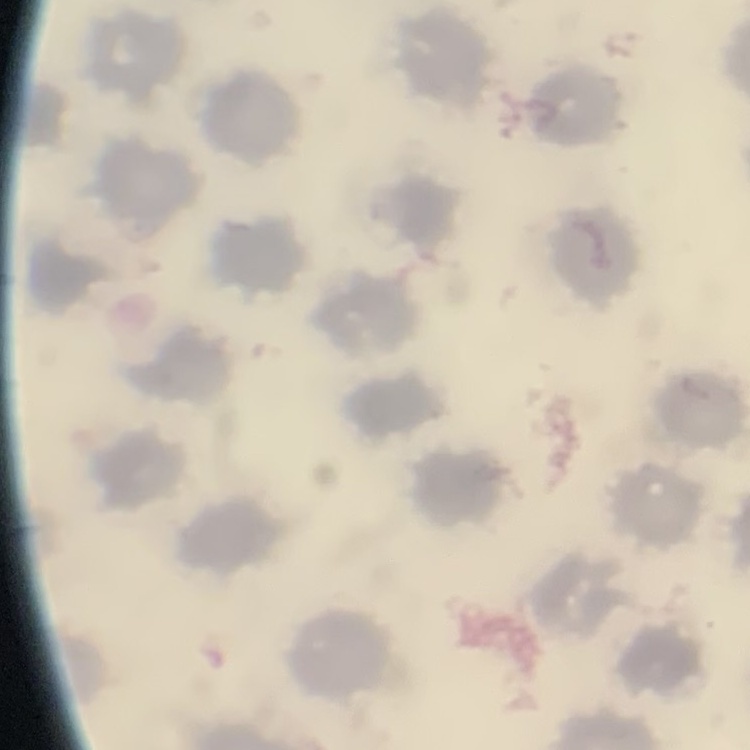
erythrocyte morphology = no rouleaux formation
image type = one tile cut from a larger photomicrograph
preparation = thin blood film
stain = Field's or Giemsa